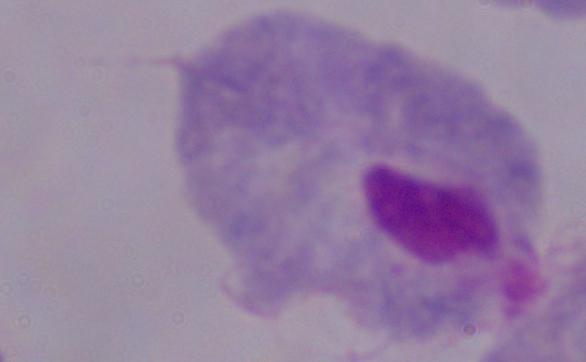
modality = micrograph
magnification = 1000x
identification = trichomonad